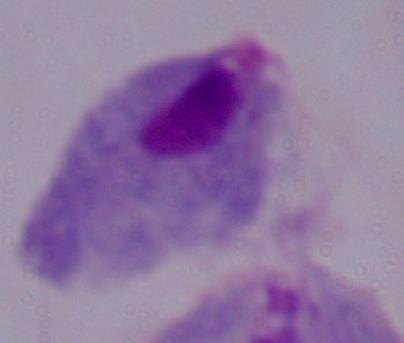
magnification = 1000x
modality = micrograph
identification = trichomonad